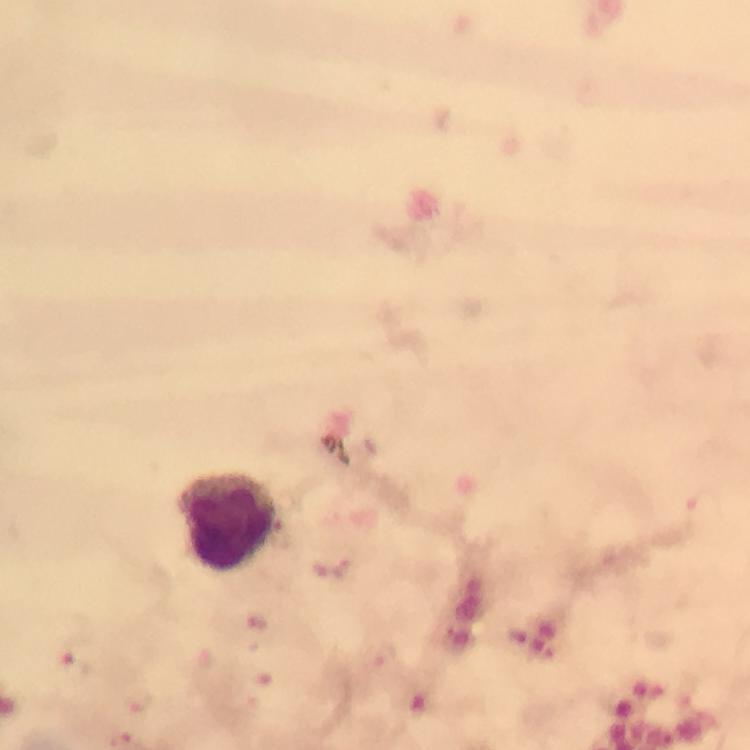

Approximate centers as {x, y} in pixels. Plasmodium parasite locations: {341, 569}, {253, 625}, {75, 667}, {140, 701}. Leukocyte locations: {226, 523}. Thick blood film. Giemsa stain. Photographed through the microscope with a smartphone camera. From a malaria diagnostic workup. Image is 750×750 pixels. 100x magnification. Immersion oil was used. A crop from one field of view.